Identify the parasite.
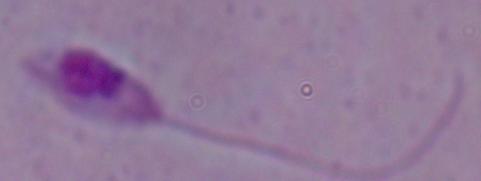
Leishmania.

1000x magnification. Micrograph.